Report the malaria status of this cell.
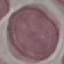
It is uninfected.

Giemsa stain. Thin blood film. Photographed with a smartphone camera at the microscope eyepiece. Cell patch, automatically extracted from a larger field of view and resized to 64 × 64 pixels.